Assess this cell for malaria.
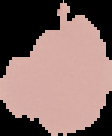
It is parasitized.

Summary:
  - Image type: cell region segmented out of the field of view; surrounding area masked to black
  - Image size: 112×136 pixels
  - Preparation: thin blood film